Comment on the morphology of the red blood cells.
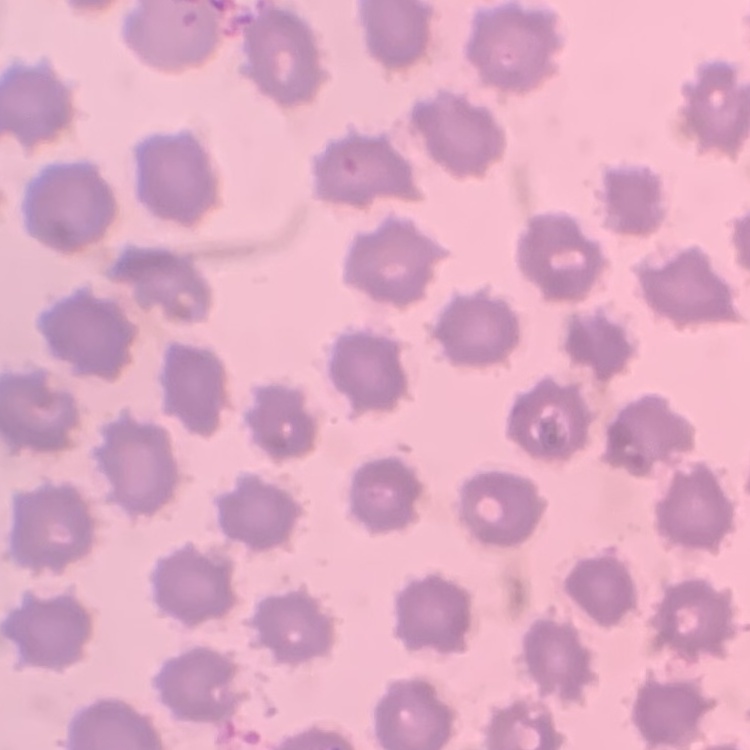
They show no rouleaux formation.

Field's or Giemsa stain. Thin peripheral smear. One tile cut from a larger photomicrograph.